Which red blood cells are P. falciparum-infected, and which are of indeterminate infection status?
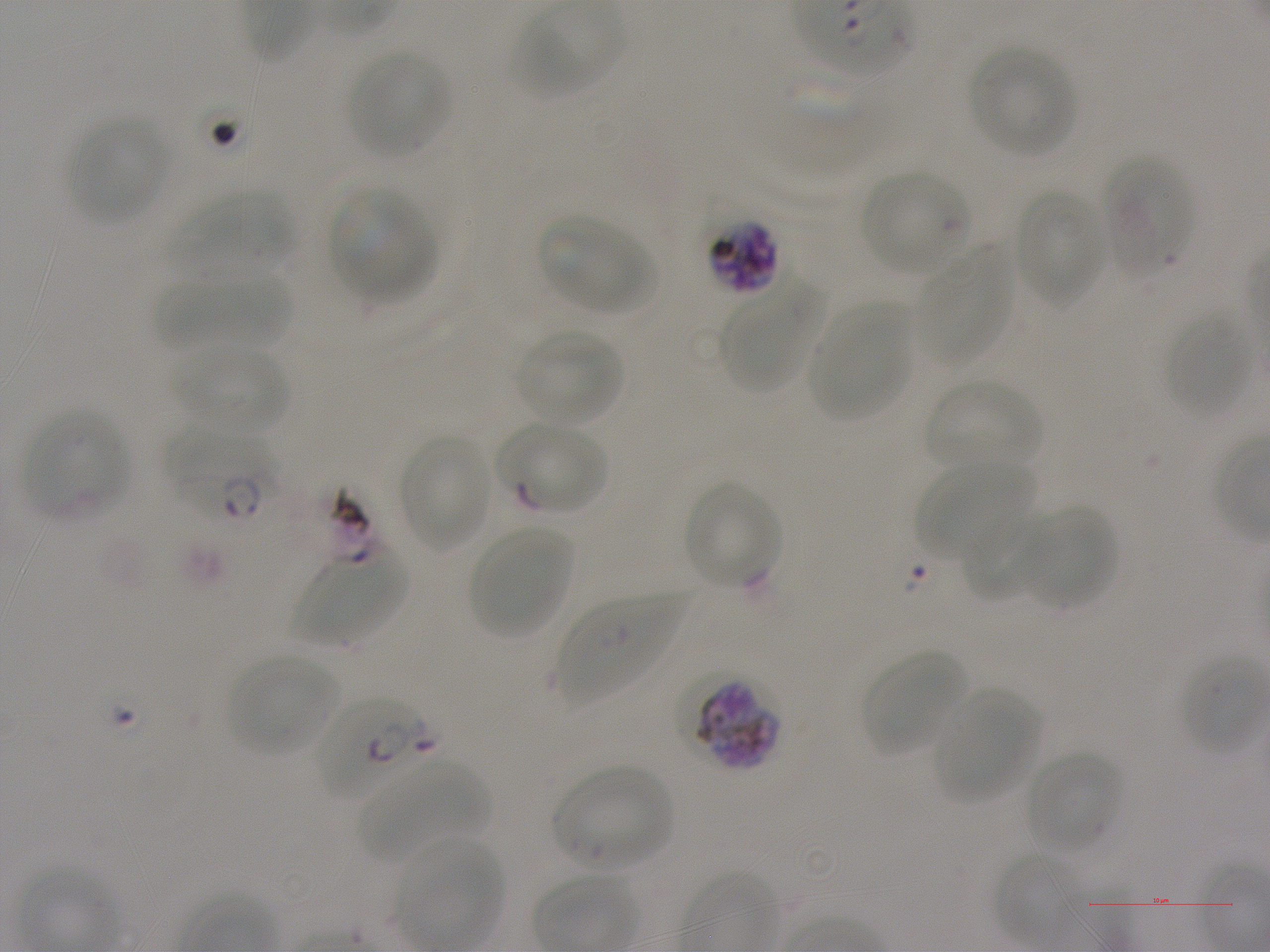
Approximate bounding boxes as {x1, y1, x2, y2} in pixels. Not every red blood cell is marked. A life-cycle stage — or a range of stages, where the recorded stages span more than one — follows each staged infected red blood cell.
Infected red blood cells: {706, 217, 780, 296} schizont; {168, 429, 278, 527}; {673, 672, 780, 772}; {314, 697, 436, 801} early ring to early trophozoite.
Red blood cells of indeterminate infection status: {504, 423, 608, 516}.

{
  "locations_of_uninfected_red_blood_cells": "{513, 4, 619, 99}, {968, 45, 1076, 157}, {347, 49, 451, 158}, {67, 116, 169, 225}, {1101, 152, 1194, 278}, {860, 171, 970, 276}, {329, 186, 435, 301}, {176, 188, 295, 270}, {1015, 189, 1106, 306}, {538, 215, 653, 313}, {916, 249, 1014, 367}, {161, 272, 291, 353}, {721, 280, 823, 390}, {810, 301, 915, 422}, {1164, 312, 1251, 418}, {516, 329, 622, 425}, {171, 344, 291, 435}, {923, 380, 1043, 474}, {23, 408, 128, 519}, {397, 434, 491, 552}, {917, 464, 1033, 561}, {682, 480, 783, 590}, {1021, 507, 1117, 611}, {959, 509, 1050, 602}, {469, 526, 575, 639}, {295, 551, 406, 645}, {557, 595, 681, 705}, {862, 650, 970, 757}, {226, 654, 340, 757}, {1179, 656, 1264, 757}, {931, 688, 1040, 803}, {1024, 751, 1123, 852}, {357, 760, 488, 861}, {553, 765, 674, 868}, {397, 838, 506, 944}, {993, 851, 1087, 946}",
  "stain": "Giemsa",
  "donor_blood_group": "A+",
  "culture": "P. falciparum strain NF54, static, in vitro",
  "preparation": "thin blood film",
  "field_of_view": "one from this slide",
  "image_size": "1270×952 pixels",
  "objective": "100x, oil immersion, numerical aperture 1.25"
}